Classify this cell by malaria status.
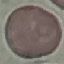
Uninfected.

image type = automatically extracted cell patch, resized to 64 × 64 pixels
capture = smartphone camera at the microscope eyepiece
stain = Giemsa
preparation = thin smear